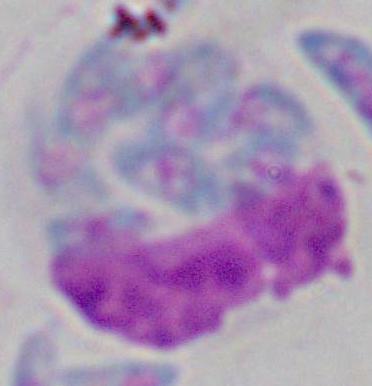

identification: white blood cell
magnification: 1000x
modality: photomicrograph